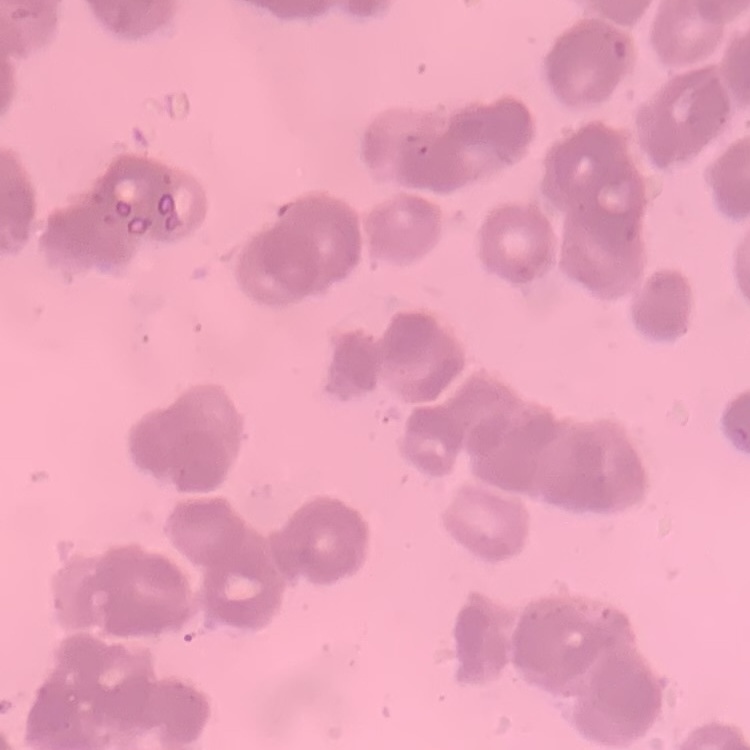

Summary:
  - Red blood cell morphology: rouleaux formation
  - Image type: square crop of a larger photomicrograph
  - Stain: Field's or Giemsa
  - Preparation: thin blood film